Comment on the morphology of the erythrocytes.
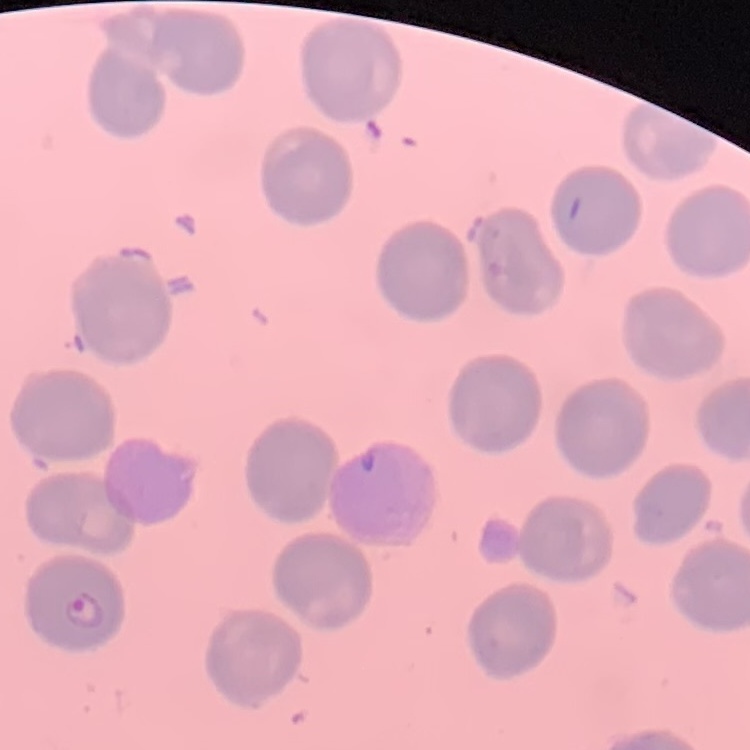

They show no rouleaux formation.

One tile cut from a larger photomicrograph. Thin peripheral smear. Field's or Giemsa stain.